Give a bounding box for every Plasmodium parasite, every leukocyte, and every artifact (stain precipitate or debris).
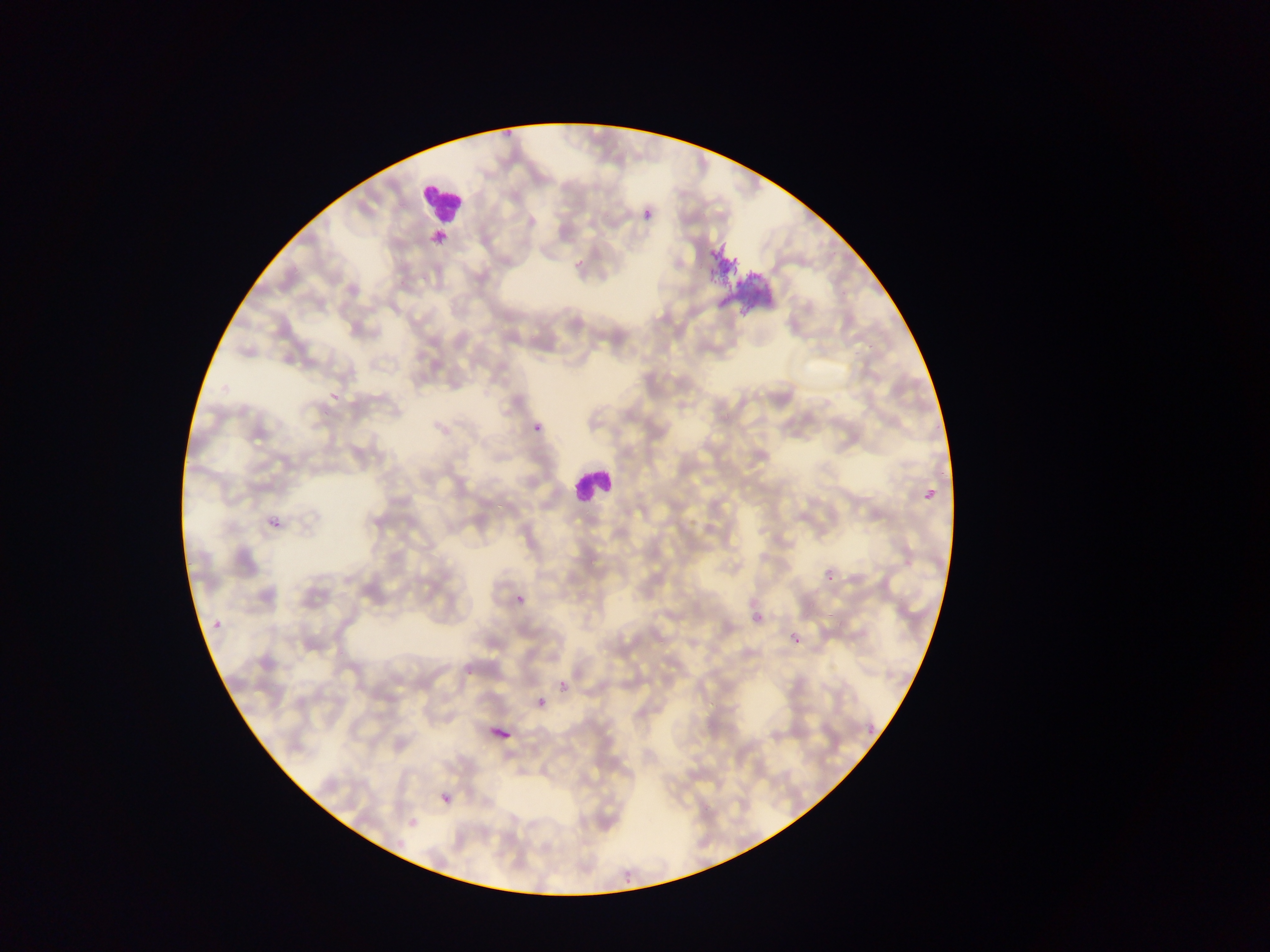
Approximate bounding boxes as [left, top, right, bottom] in pixels.
Plasmodium parasites: [635, 207, 653, 225], [326, 392, 347, 404], [532, 417, 543, 435], [263, 510, 285, 531], [514, 592, 526, 606], [208, 606, 226, 625], [753, 614, 761, 622], [792, 635, 800, 644], [557, 680, 569, 693], [442, 793, 451, 803].
Leukocytes: [422, 178, 467, 223], [570, 462, 613, 505].
Artifacts (stain precipitate or debris): [699, 228, 777, 327].

Summary:
  - Image size: 1270×952 pixels
  - Preparation: thin blood film
  - Field of view: single
  - Capture: mobile-phone photograph through a microscope
  - Country: Ghana